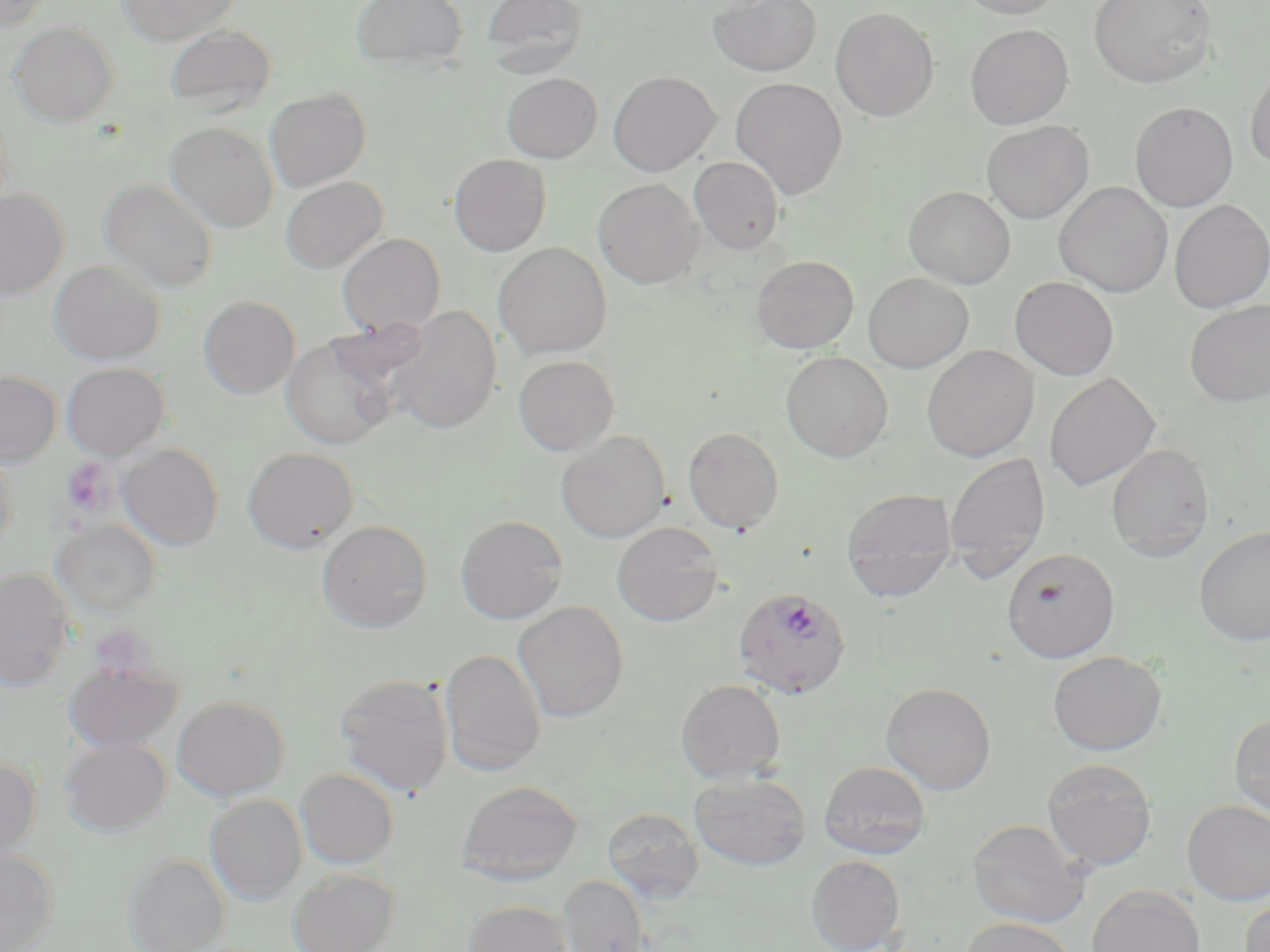
Summary:
  - Coordinate format: approximate bounding boxes as [x1, y1, x2, y2] in pixels
  - Uninfected red blood cell locations: [0, 0, 49, 34], [117, 0, 243, 45], [351, 0, 468, 71], [482, 0, 587, 77], [708, 0, 822, 76], [956, 0, 1068, 18], [1089, 0, 1218, 88], [831, 7, 939, 122], [10, 22, 118, 126], [164, 23, 277, 115], [965, 24, 1074, 129], [1245, 61, 1270, 171], [608, 70, 721, 176], [502, 73, 602, 163], [730, 77, 848, 199], [264, 88, 371, 191], [1130, 101, 1238, 212], [981, 120, 1094, 224], [165, 122, 278, 232], [449, 154, 551, 256], [689, 156, 785, 254], [280, 176, 388, 273], [594, 178, 705, 289], [99, 179, 219, 293], [1053, 181, 1173, 297], [904, 186, 1016, 289], [0, 189, 69, 298], [1169, 199, 1270, 312], [338, 233, 446, 336], [493, 242, 612, 359], [752, 255, 858, 353], [49, 260, 165, 364], [863, 272, 973, 372], [1010, 276, 1119, 380], [198, 295, 300, 398], [1184, 299, 1270, 406], [386, 306, 502, 434], [281, 334, 398, 450], [922, 345, 1039, 461], [781, 351, 893, 462], [514, 355, 619, 455], [61, 362, 169, 460], [0, 370, 61, 466], [1044, 372, 1160, 492], [683, 427, 784, 533], [556, 430, 671, 542], [119, 443, 224, 550], [1106, 443, 1215, 562], [242, 446, 359, 553], [0, 450, 19, 554], [944, 451, 1050, 579], [841, 487, 959, 601], [455, 514, 568, 624], [52, 520, 161, 615], [317, 520, 433, 633], [612, 521, 723, 626], [1194, 525, 1270, 645], [1002, 547, 1119, 662], [0, 567, 76, 690], [513, 601, 629, 722], [440, 649, 546, 775], [1048, 650, 1167, 754], [64, 662, 182, 752], [333, 672, 454, 796], [676, 679, 786, 784], [881, 681, 996, 794], [172, 695, 289, 800], [1230, 714, 1270, 822], [61, 737, 170, 836], [0, 756, 42, 863], [1041, 758, 1158, 871], [819, 761, 931, 859], [296, 769, 399, 868], [690, 773, 810, 870], [457, 779, 582, 884], [205, 794, 307, 905], [1182, 799, 1270, 905], [602, 806, 703, 902], [968, 819, 1091, 928], [0, 848, 60, 951], [124, 852, 231, 952], [807, 855, 906, 952], [287, 868, 398, 952], [559, 874, 650, 951], [1087, 884, 1206, 952], [1240, 894, 1270, 952], [463, 900, 573, 952], [960, 918, 1078, 952]
  - Plasmodium falciparum-infected red blood cell locations: [733, 587, 851, 698]
  - Platelet locations: [60, 458, 113, 516]
  - Slide-level diagnosis: Plasmodium falciparum
  - Image size: 1270×952 pixels
  - Field of view: single
  - Stain: May-Grünwald-Giemsa
  - Magnification: 1000x
  - Modality: optical microscopy
  - Preparation: thin blood smear